Report the malaria status of this cell.
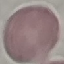
Uninfected.

Summary:
  - Capture: smartphone camera at the microscope eyepiece
  - Image type: cell patch, automatically extracted from a larger field of view and resized to 64 × 64 pixels
  - Stain: Giemsa
  - Preparation: thin blood film